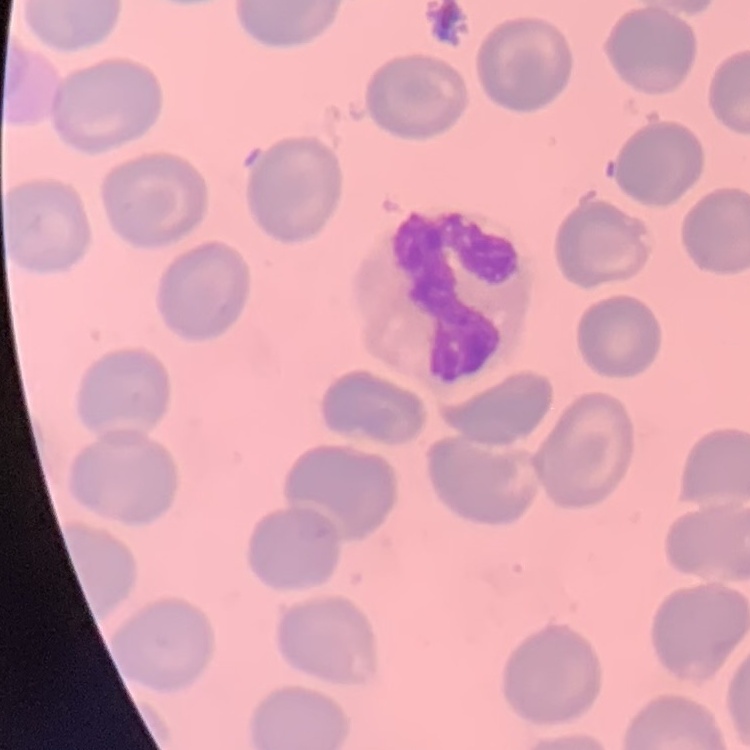
red blood cell morphology = no rouleaux formation
stain = Field's or Giemsa
image type = one tile cut from a larger photomicrograph
preparation = thin blood film